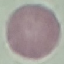

Summary:
  - Result: no malaria parasites detected
  - Preparation: thin smear
  - Image type: automatically extracted cell patch, resized to 64 × 64 pixels
  - Capture: smartphone through the microscope eyepiece
  - Stain: Giemsa